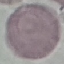
Summary:
  - Result: no malaria parasites detected
  - Stain: Giemsa
  - Image type: cell patch, automatically extracted from a larger field of view and resized to 64 × 64 pixels
  - Preparation: thin blood film
  - Capture: smartphone through the microscope eyepiece